Assess the morphology of the erythrocytes.
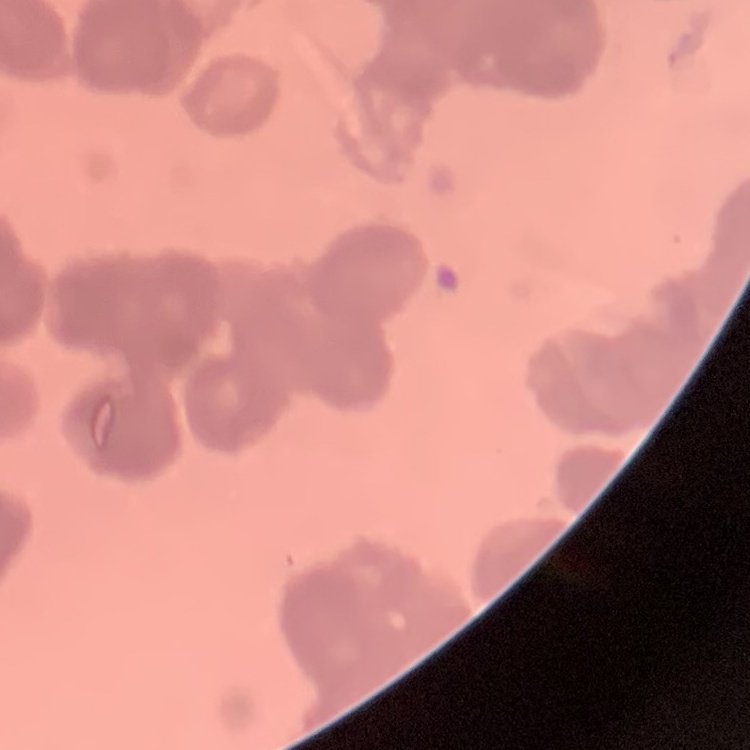

Rouleaux formation.

Square crop of a larger photomicrograph. Thin blood smear. Stained with either Field's or Giemsa.